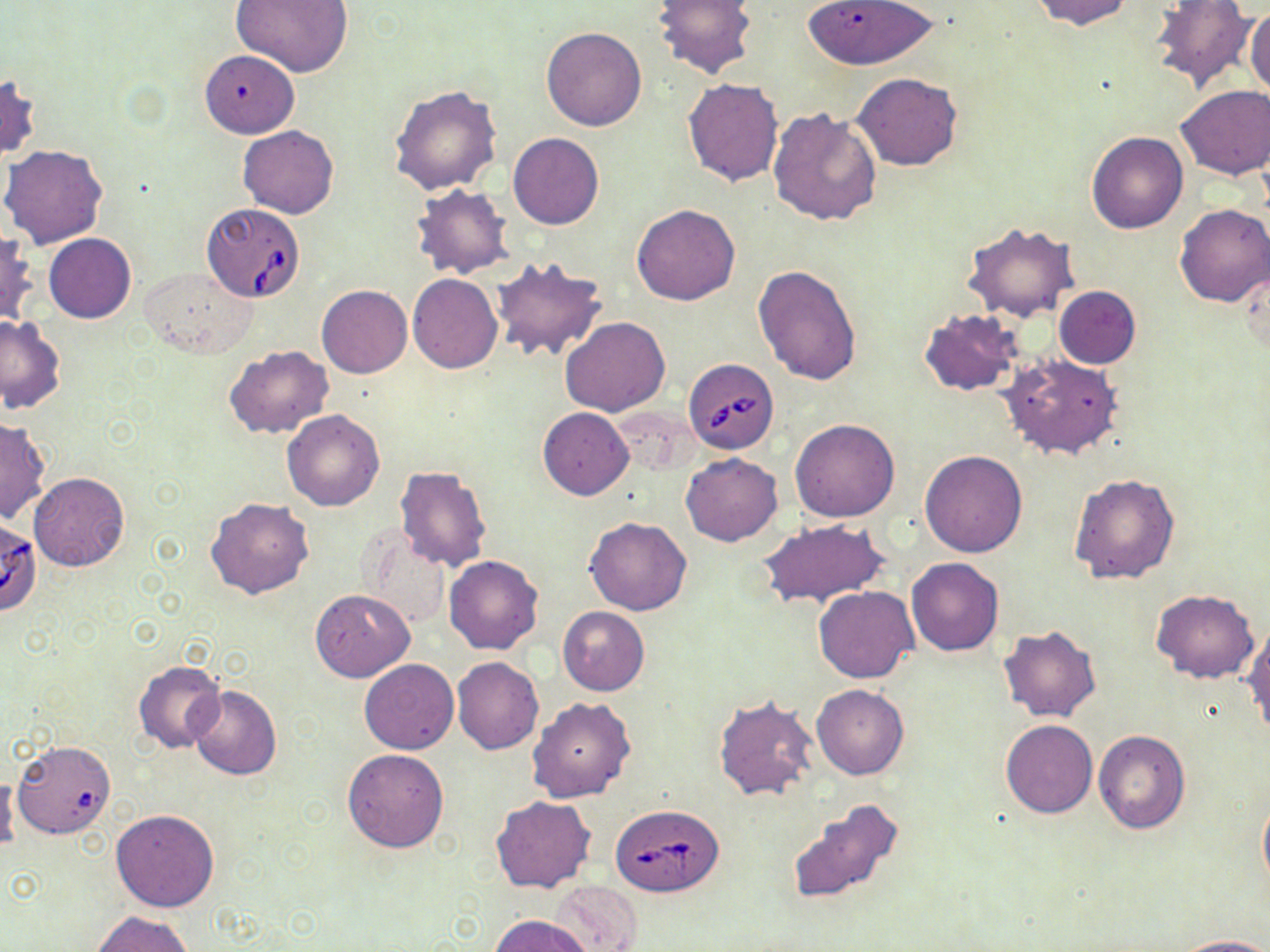
Summary:
  - Coordinate format: approximate bounding boxes as named x1/y1/x2/y2 corners in pixels
  - Uninfected red blood cell locations: (x1=232, y1=0, x2=352, y2=77), (x1=652, y1=0, x2=759, y2=81), (x1=800, y1=0, x2=940, y2=70), (x1=1031, y1=0, x2=1137, y2=32), (x1=1149, y1=2, x2=1256, y2=92), (x1=1245, y1=7, x2=1270, y2=99), (x1=541, y1=26, x2=647, y2=131), (x1=200, y1=50, x2=299, y2=137), (x1=853, y1=72, x2=964, y2=171), (x1=1, y1=73, x2=39, y2=163), (x1=683, y1=78, x2=784, y2=185), (x1=389, y1=84, x2=502, y2=193), (x1=1174, y1=85, x2=1269, y2=180), (x1=767, y1=107, x2=882, y2=226), (x1=239, y1=124, x2=338, y2=218), (x1=1086, y1=131, x2=1188, y2=233), (x1=508, y1=132, x2=604, y2=229), (x1=1, y1=143, x2=108, y2=249), (x1=410, y1=183, x2=514, y2=279), (x1=631, y1=203, x2=739, y2=306), (x1=1175, y1=204, x2=1270, y2=308), (x1=963, y1=222, x2=1079, y2=323), (x1=0, y1=232, x2=38, y2=326), (x1=44, y1=233, x2=136, y2=322), (x1=488, y1=255, x2=607, y2=363), (x1=1237, y1=263, x2=1268, y2=360), (x1=753, y1=264, x2=861, y2=386), (x1=141, y1=266, x2=257, y2=357), (x1=408, y1=273, x2=503, y2=373), (x1=316, y1=284, x2=412, y2=378), (x1=1054, y1=286, x2=1142, y2=368), (x1=918, y1=308, x2=1023, y2=396), (x1=0, y1=316, x2=66, y2=414), (x1=559, y1=317, x2=670, y2=417), (x1=224, y1=345, x2=334, y2=439), (x1=1000, y1=353, x2=1126, y2=460), (x1=537, y1=407, x2=634, y2=500), (x1=282, y1=409, x2=385, y2=512), (x1=0, y1=416, x2=50, y2=524), (x1=790, y1=419, x2=901, y2=522), (x1=921, y1=451, x2=1026, y2=557), (x1=681, y1=453, x2=782, y2=546), (x1=394, y1=465, x2=491, y2=571), (x1=28, y1=471, x2=130, y2=571), (x1=1069, y1=472, x2=1180, y2=586), (x1=205, y1=496, x2=315, y2=599), (x1=584, y1=518, x2=692, y2=615), (x1=758, y1=518, x2=891, y2=610), (x1=356, y1=526, x2=452, y2=629), (x1=443, y1=555, x2=543, y2=653), (x1=906, y1=557, x2=1004, y2=656), (x1=813, y1=585, x2=919, y2=683), (x1=310, y1=588, x2=414, y2=682), (x1=1151, y1=589, x2=1259, y2=683), (x1=557, y1=606, x2=649, y2=695), (x1=1242, y1=623, x2=1269, y2=735), (x1=997, y1=624, x2=1101, y2=722), (x1=452, y1=656, x2=544, y2=754), (x1=132, y1=659, x2=227, y2=754), (x1=359, y1=659, x2=458, y2=754), (x1=812, y1=683, x2=908, y2=780), (x1=187, y1=686, x2=283, y2=781), (x1=712, y1=695, x2=818, y2=801), (x1=527, y1=697, x2=636, y2=803), (x1=1001, y1=719, x2=1097, y2=818), (x1=1092, y1=729, x2=1189, y2=834), (x1=12, y1=741, x2=116, y2=839), (x1=342, y1=748, x2=450, y2=852), (x1=0, y1=771, x2=20, y2=858), (x1=1258, y1=793, x2=1270, y2=893), (x1=491, y1=796, x2=596, y2=893), (x1=785, y1=800, x2=907, y2=912), (x1=111, y1=809, x2=220, y2=912), (x1=547, y1=880, x2=643, y2=951), (x1=91, y1=911, x2=195, y2=952), (x1=491, y1=915, x2=594, y2=952), (x1=1172, y1=935, x2=1270, y2=952)
  - Babesia divergens-infected red blood cell locations: (x1=200, y1=202, x2=306, y2=301), (x1=683, y1=359, x2=779, y2=454), (x1=1, y1=517, x2=42, y2=614), (x1=611, y1=805, x2=723, y2=896)
  - Slide-level diagnosis: Babesia divergens
  - Magnification: 1000x
  - Image size: 1270×952 pixels
  - Modality: light microscopy
  - Stain: May-Grünwald-Giemsa
  - Preparation: thin blood smear
  - Field of view: single